Report the malaria status of this cell.
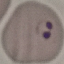
Parasitized.

Summary:
  - Capture: smartphone through the microscope eyepiece
  - Image type: cell patch, automatically extracted from a larger field of view and resized to 64 × 64 pixels
  - Stain: Giemsa
  - Preparation: thin blood smear